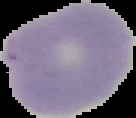 Malaria status: uninfected. Segmented cell region on a black background. Image is 136×118 pixels. From a thin blood film.